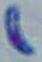
Micrograph. Toxoplasma gondii is shown. 1000x magnification.